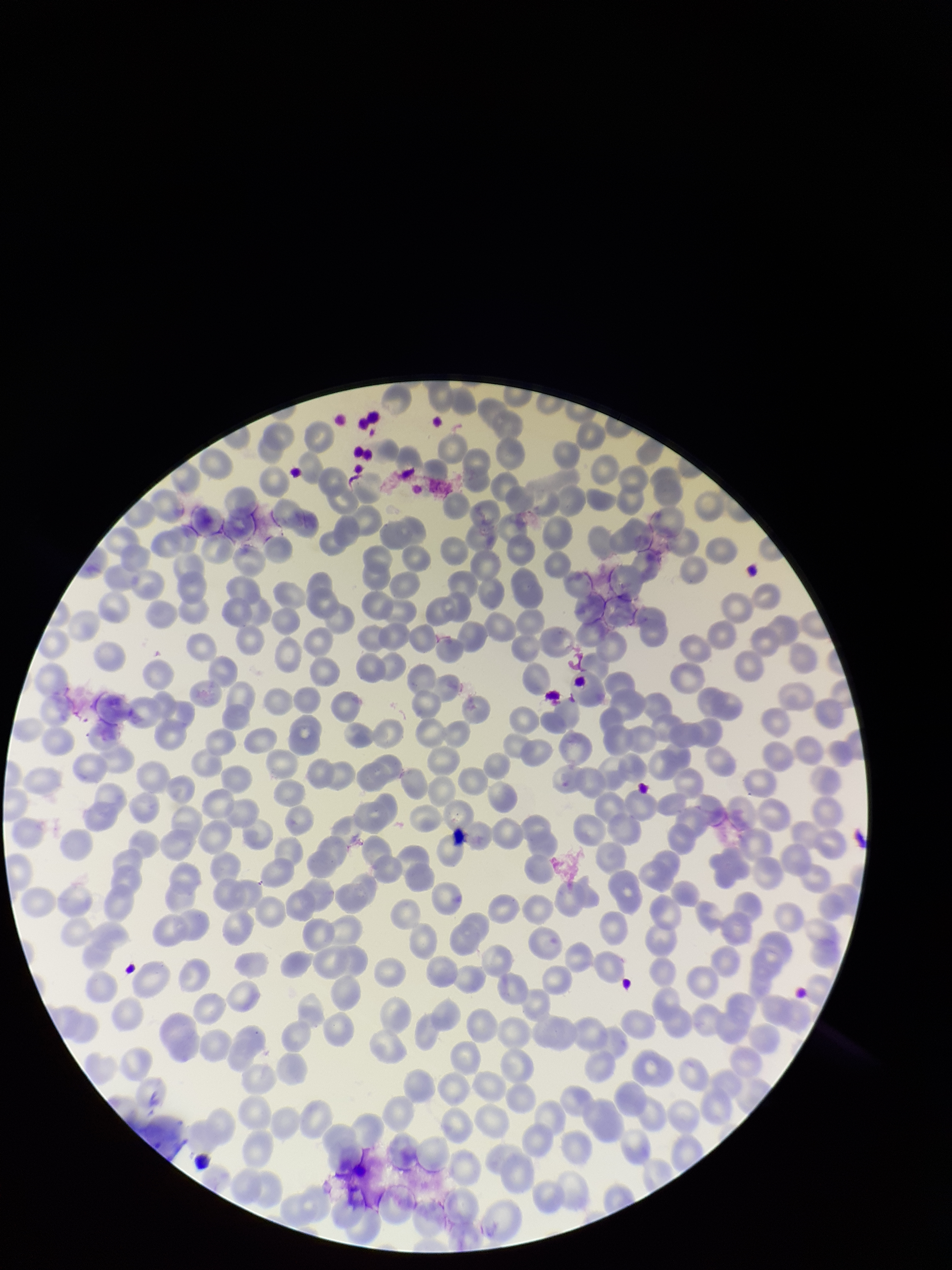 Smartphone photograph taken through the eyepiece of a microscope. Parasitized red blood cells: none seen. Patient malaria status: positive. Parasitized red blood cell count: 0. Image is 952×1270 pixels. One field from this slide. Preparation: thin. Species reported for this patient: Plasmodium falciparum. Red blood cell count: 241. Giemsa stain.